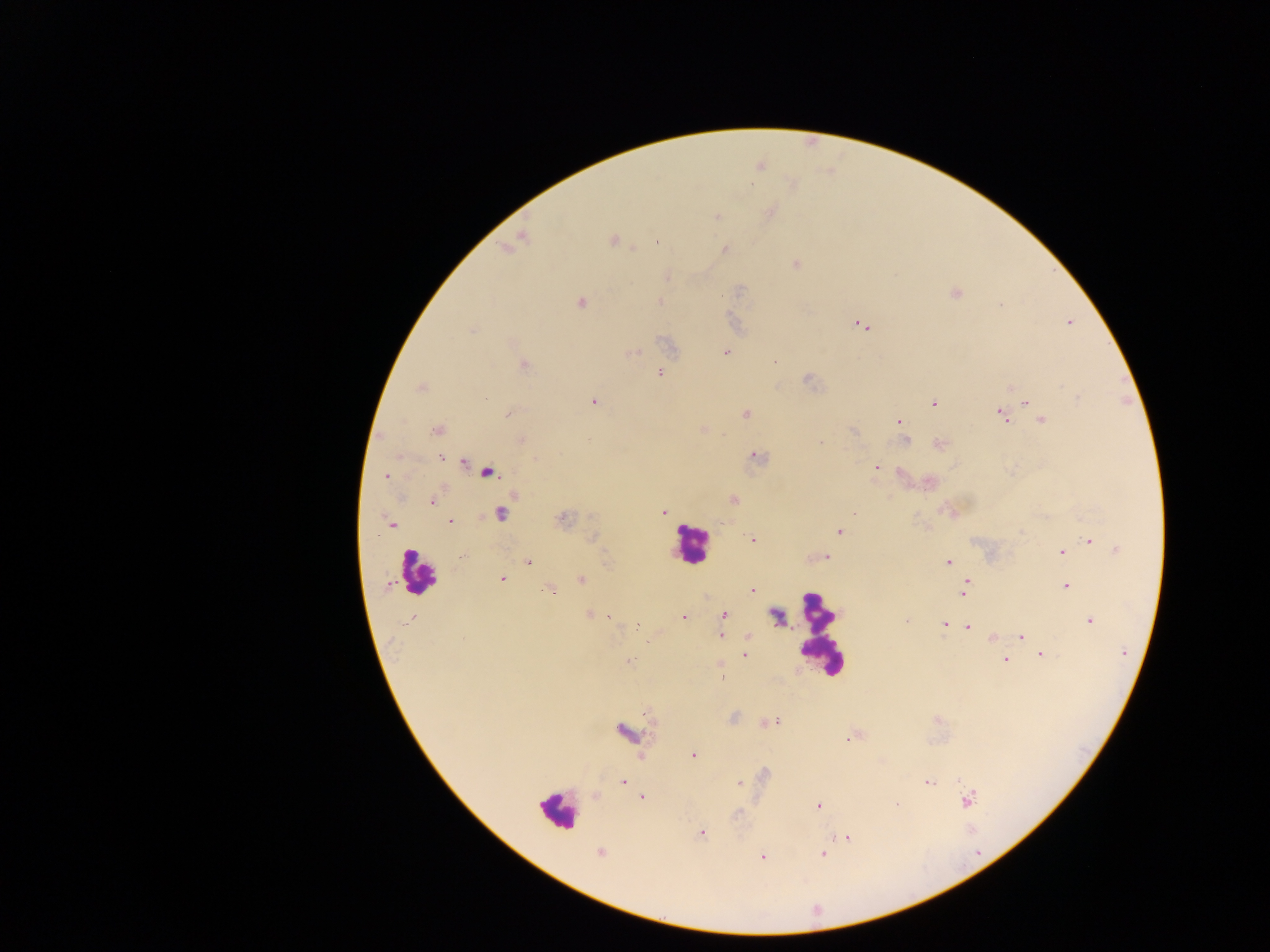
Approximate centers as {x, y} in pixels. Leukocyte locations: {692, 544}, {417, 573}, {816, 635}, {558, 810}. Malaria parasite locations: {759, 166}, {769, 212}, {717, 216}, {518, 238}, {613, 241}, {657, 241}, {508, 246}, {724, 249}, {796, 264}, {954, 293}, {659, 301}, {581, 302}, {1069, 322}, {860, 324}, {725, 352}, {631, 353}, {774, 361}, {523, 364}, {661, 372}, {806, 378}, {1010, 386}, {421, 387}, {594, 401}, {933, 402}, {1025, 402}, {1032, 406}, {509, 413}, {746, 414}, {1001, 415}, {1042, 419}, {898, 422}, {702, 428}, {437, 429}, {852, 431}, {520, 439}, {590, 439}, {905, 441}, {939, 443}, {439, 455}, {754, 456}, {464, 463}, {876, 468}, {487, 472}, {900, 472}, {386, 476}, {929, 481}, {732, 499}, {433, 501}, {663, 511}, {952, 511}, {500, 513}, {562, 519}, {449, 521}, {391, 524}, {839, 531}, {752, 539}, {1089, 541}, {1117, 550}, {1060, 551}, {826, 557}, {527, 562}, {948, 562}, {502, 579}, {582, 580}, {1065, 585}, {965, 587}, {549, 589}, {752, 589}, {589, 615}, {723, 615}, {776, 615}, {610, 616}, {683, 616}, {1089, 620}, {907, 621}, {945, 624}, {968, 627}, {721, 635}, {747, 636}, {1021, 636}, {993, 637}, {744, 654}, {1040, 654}, {1005, 660}, {628, 661}, {719, 662}, {722, 678}, {769, 722}, {623, 732}, {851, 737}, {692, 755}, {622, 782}, {740, 783}, {929, 783}, {596, 796}, {641, 797}, {967, 800}, {895, 804}, {818, 806}, {701, 832}, {846, 836}, {599, 852}, {822, 854}, {763, 856}. One field of view. Mobile-phone photograph taken through the microscope. Image is 1270×952 pixels. Thick blood film. Sample from Ghana.